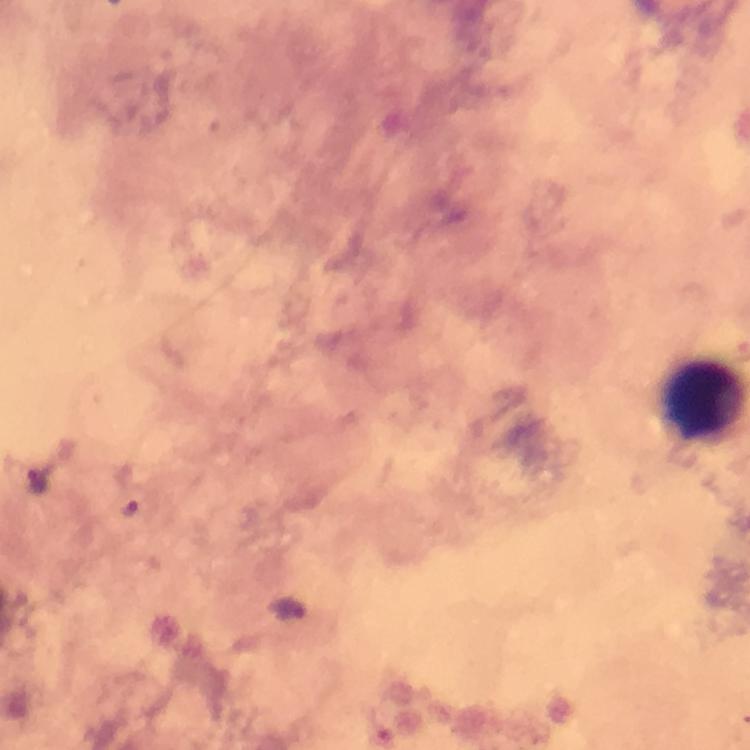
Approximate centers as {x, y} in pixels.
Summary:
  - Leukocyte locations: {701, 400}
  - Malaria parasite locations: {38, 480}, {128, 507}, {289, 610}
  - Cropped from: one field of view
  - Context: from a diagnostic examination for malaria
  - Immersion oil: applied
  - Stain: Giemsa
  - Capture: smartphone mounted on the microscope
  - Preparation: thick smear
  - Magnification: 100x
  - Image size: 750×750 pixels